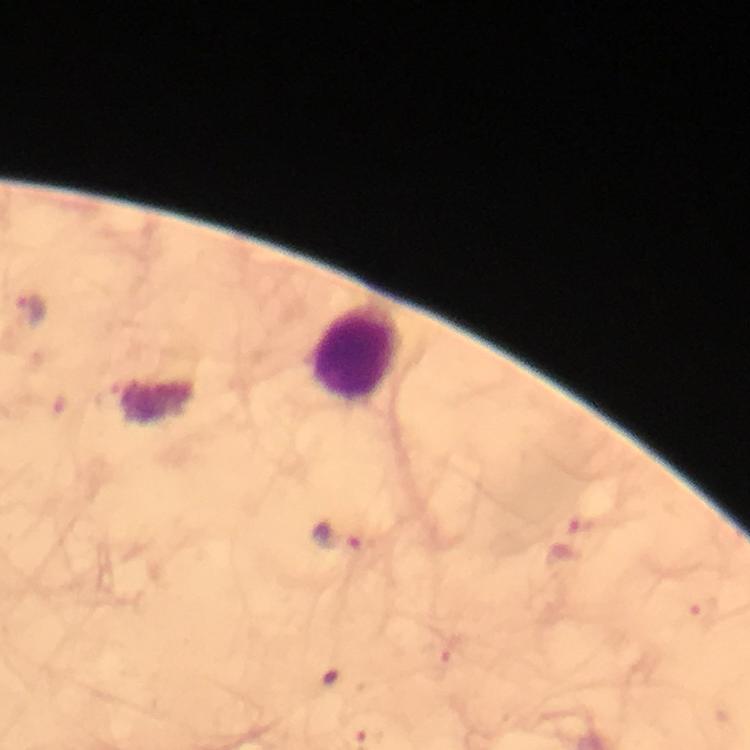

Approximate centers as (x, y) in pixels.
Summary:
  - Plasmodium parasite locations: (30, 313), (587, 525), (341, 537), (706, 614), (438, 663)
  - Leukocyte locations: (358, 352)
  - Immersion oil: used
  - Cropped from: one field of view
  - Image size: 750×750 pixels
  - Context: from a malaria diagnostic workup
  - Preparation: thick smear
  - Stain: Giemsa
  - Capture: smartphone camera through the microscope
  - Magnification: 100x